Report the malaria status of this cell.
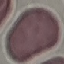
It is uninfected.

Summary:
  - Stain: Giemsa
  - Capture: smartphone camera at the microscope eyepiece
  - Image type: automatically extracted cell patch, resized to 64 × 64 pixels
  - Preparation: thin smear